Give the position of every malaria parasite.
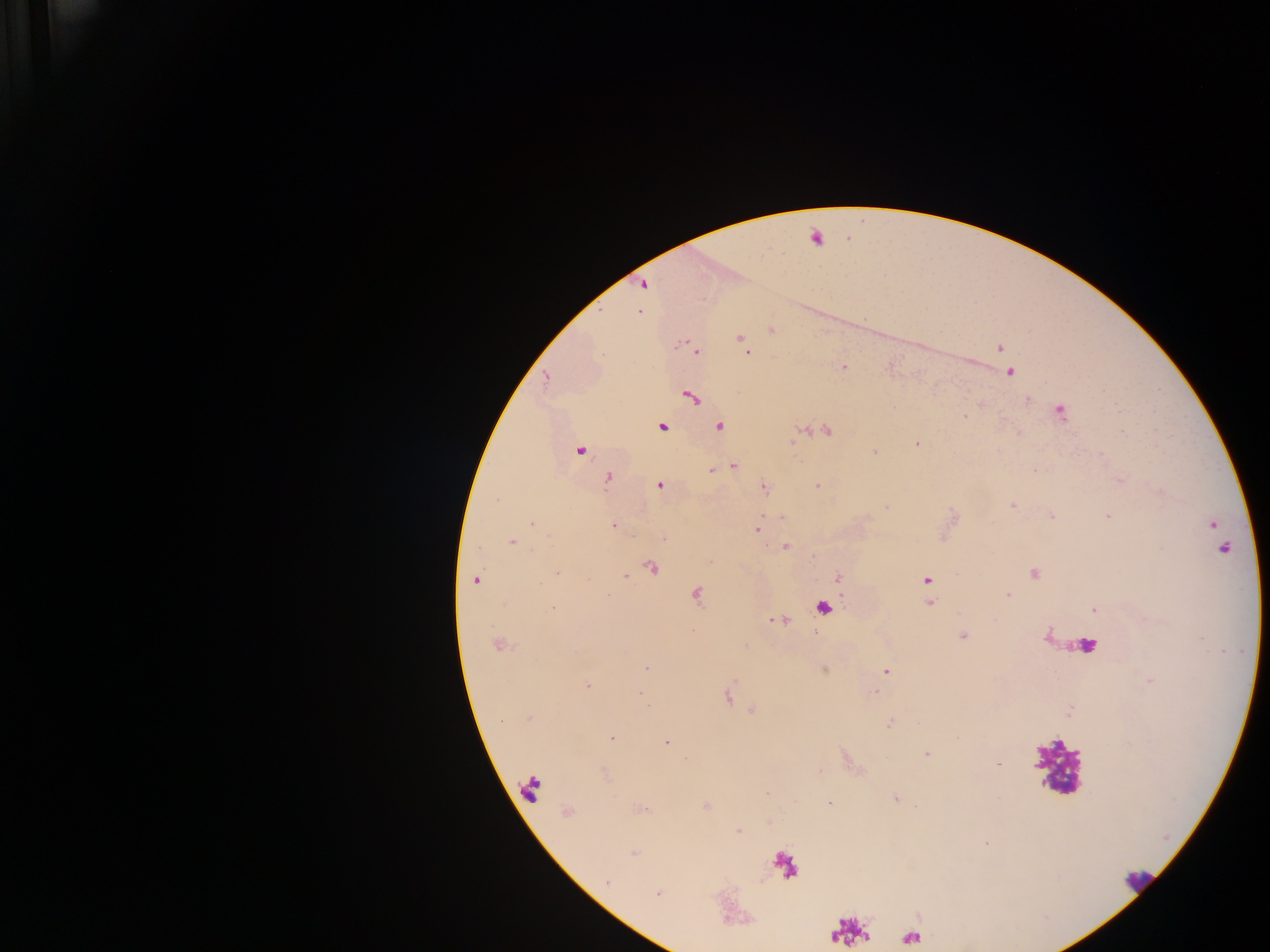
Approximate centers as x y in pixels.
Malaria parasites: 644 285; 638 311; 772 330; 740 338; 1000 348; 697 351; 747 352; 843 367; 1011 373; 546 378; 691 397; 1027 399; 1061 411; 663 426; 720 426; 828 431; 917 444; 580 451; 875 452; 733 466; 713 470; 608 477; 660 485; 763 486; 817 486; 1012 505; 1051 516; 781 517; 1107 517; 532 523; 1213 524; 612 526; 756 529; 664 538; 511 541; 785 547; 1224 548; 652 567; 557 572; 1034 573; 625 575; 838 577; 475 580; 926 580; 696 595; 1008 595; 930 602; 824 608; 553 609; 1094 609; 777 620; 963 637; 497 645; 646 668; 886 672; 587 686; 876 692; 640 693; 528 718; 889 723; 612 738; 665 743; 926 754; 998 764; 895 799; 829 802; 706 806; 738 831; 634 854; 608 882; 657 894.

preparation: thick blood film
country: Ghana
field_of_view: single
leukocyte_locations: 'approximate centers as x y in pixels: 1083 645; 1057 767; 1137 882'
image_size: 1270×952 pixels
capture: mobile-phone photograph through a microscope